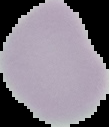 Segmented cell region on a black background. Image is 109×127 pixels. Result: no Plasmodium parasites detected. From a thin blood film.